Report the malaria status of this cell.
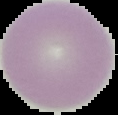
It is uninfected.

Cell region segmented out of the field of view; the surrounding area is masked to black. Image is 118×115 pixels. From a thin blood film.